State which parasite is depicted.
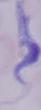

A trypanosome.

{
  "magnification": "1000x",
  "modality": "micrograph"
}